Report the malaria status of this cell.
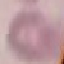

It is uninfected.

Giemsa stain. Thin blood film. Acquired by smartphone through the microscope eyepiece. Cell patch, automatically extracted from a larger field of view and resized to 64 × 64 pixels.